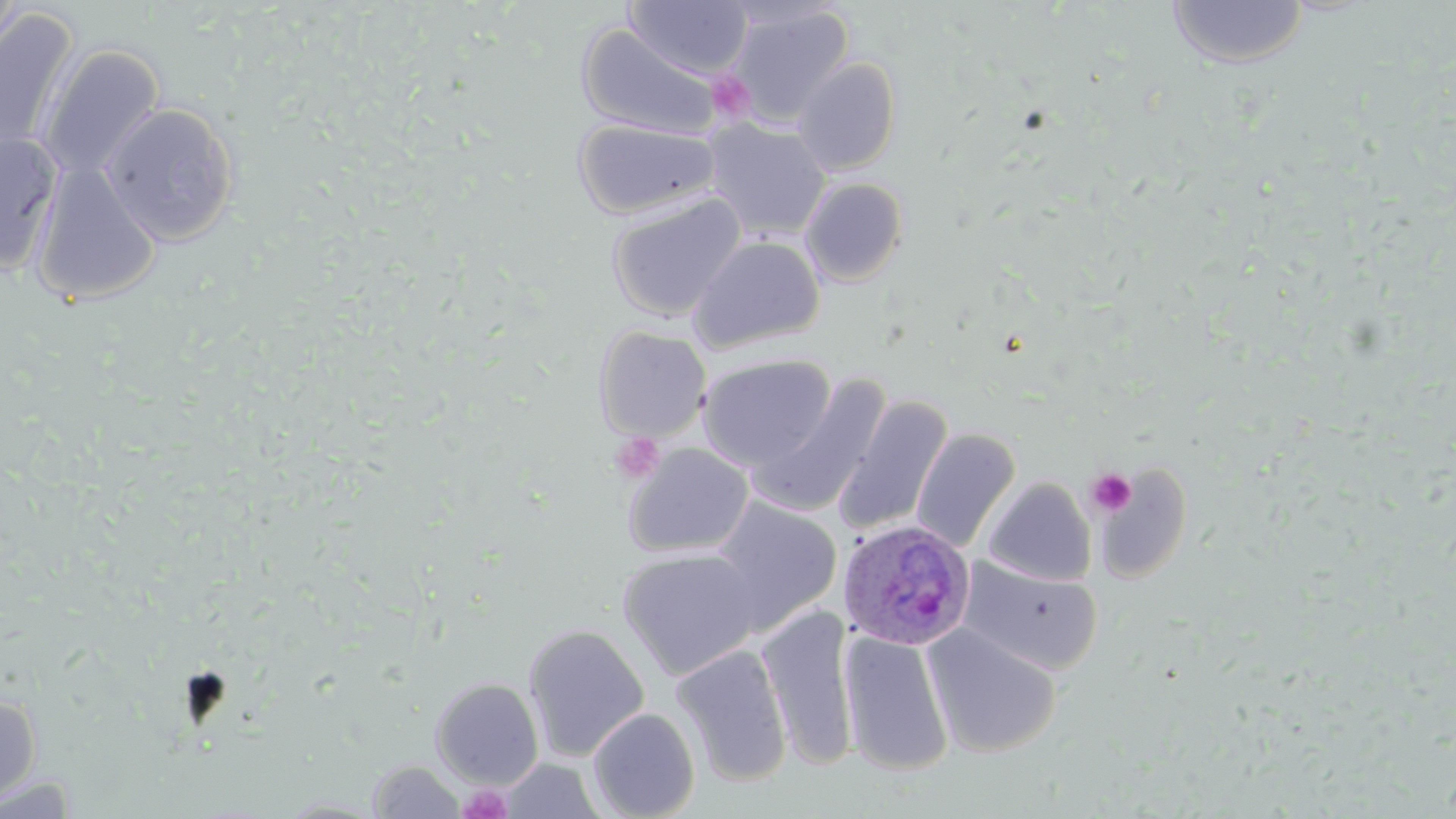

Summary:
  - Coordinate format: approximate bounding boxes as (x1,y1)-(x2,y2) corner pairs in pixels
  - Platelet locations: (707,70)-(757,125), (610,432)-(665,483), (1085,468)-(1137,518), (457,784)-(513,819)
  - Plasmodium ovale-infected red blood cell locations: (838,518)-(976,651)
  - Uninfected red blood cell locations: (0,0)-(29,65), (623,1)-(753,80), (1167,1)-(1309,68), (725,4)-(855,127), (0,8)-(80,162), (575,23)-(722,140), (39,44)-(165,181), (792,56)-(901,175), (102,102)-(239,245), (573,117)-(721,220), (702,119)-(831,240), (0,133)-(63,275), (29,160)-(162,306), (799,177)-(908,286), (606,193)-(746,321), (689,235)-(826,353), (593,325)-(712,442), (697,354)-(837,470), (746,375)-(892,519), (833,395)-(954,539), (911,428)-(1020,554), (624,442)-(755,558), (982,476)-(1096,586), (711,495)-(843,632), (618,548)-(763,680), (959,557)-(1103,675), (757,605)-(859,769), (522,623)-(650,761), (923,623)-(1061,758), (839,630)-(953,775), (673,644)-(793,787), (431,677)-(544,788), (0,692)-(43,806), (587,707)-(700,819), (499,758)-(606,818), (367,760)-(466,818), (0,772)-(84,817)
  - Slide-level diagnosis: Plasmodium ovale
  - Image size: 1456×819 pixels
  - Field of view: one of a larger specimen
  - Magnification: 1000x
  - Stain: May-Grünwald-Giemsa
  - Preparation: thin blood smear
  - Modality: light microscopy